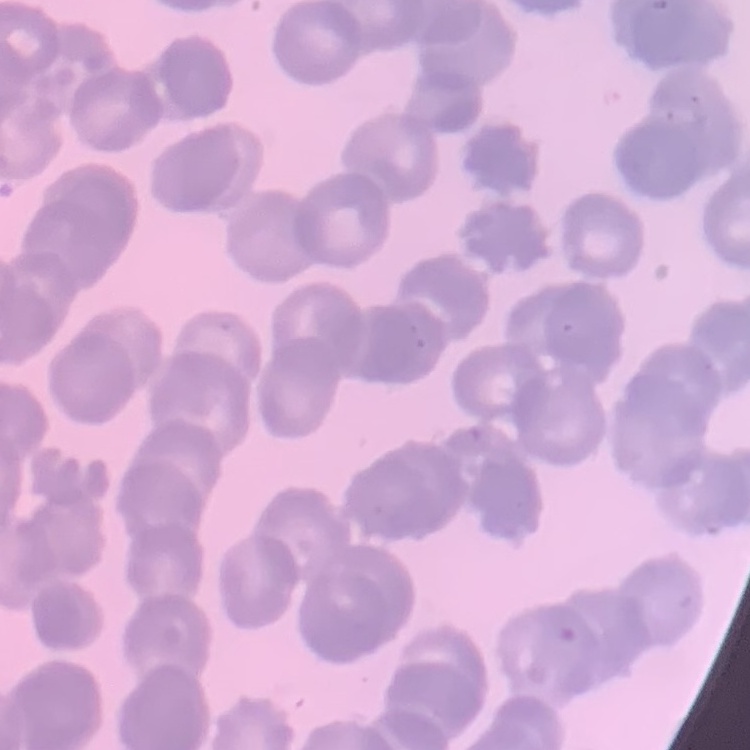
Summary:
  - Erythrocyte morphology: rouleaux formation
  - Preparation: thin blood film
  - Image type: square crop of a larger photomicrograph
  - Stain: Field's or Giemsa